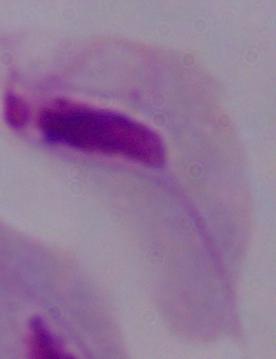

modality = photomicrograph
magnification = 1000x
identification = trichomonad